Locate every uninfected red blood cell.
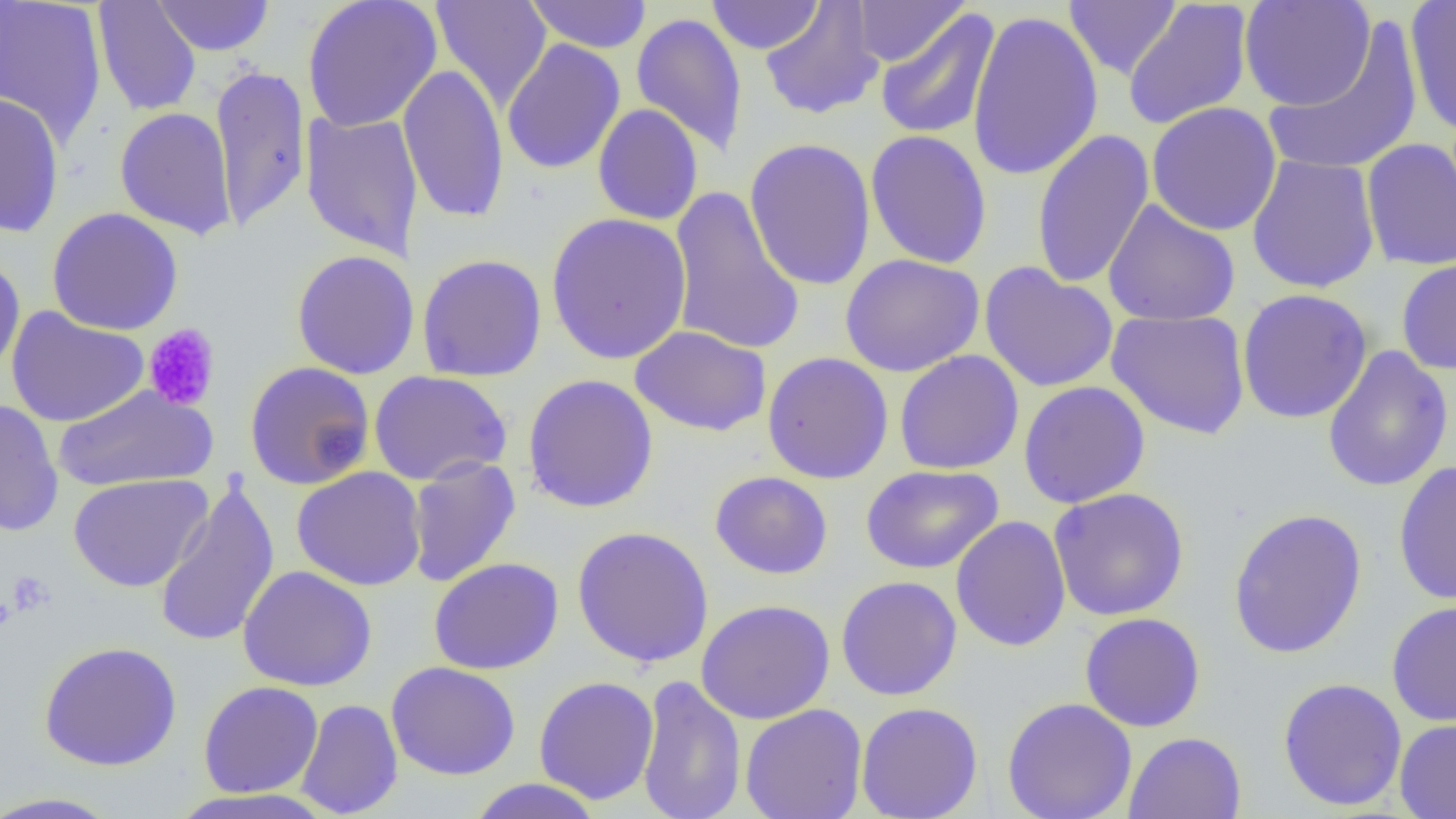
Approximate bounding boxes as [x1, y1, x2, y2] in pixels.
Uninfected red blood cells: [92, 0, 202, 117], [152, 0, 275, 56], [302, 0, 442, 132], [431, 0, 551, 111], [524, 0, 653, 53], [705, 0, 824, 54], [1064, 0, 1181, 80], [1239, 0, 1375, 111], [1404, 0, 1456, 138], [0, 1, 108, 146], [759, 1, 885, 120], [851, 1, 968, 67], [1122, 1, 1254, 131], [875, 8, 1001, 141], [966, 9, 1104, 182], [630, 13, 748, 158], [1263, 19, 1423, 179], [501, 39, 626, 175], [397, 63, 510, 224], [209, 64, 311, 231], [0, 91, 65, 238], [1146, 101, 1282, 236], [592, 104, 704, 226], [114, 107, 236, 239], [300, 112, 423, 260], [1031, 128, 1155, 290], [865, 129, 993, 270], [744, 137, 877, 292], [1361, 138, 1456, 271], [1246, 154, 1381, 294], [667, 185, 805, 356], [1103, 198, 1241, 327], [46, 207, 184, 336], [546, 212, 692, 365], [291, 250, 420, 379], [416, 253, 547, 382], [840, 253, 984, 377], [0, 255, 26, 381], [1396, 256, 1456, 376], [978, 262, 1119, 393], [1237, 288, 1373, 424], [6, 307, 150, 427], [1106, 309, 1250, 439], [630, 325, 772, 437], [1322, 346, 1453, 493], [893, 349, 1024, 474], [761, 351, 894, 484], [244, 361, 376, 490], [369, 370, 512, 485], [522, 373, 659, 513], [1018, 380, 1151, 508], [53, 384, 218, 491], [0, 399, 64, 537], [405, 456, 521, 588], [1393, 460, 1456, 606], [861, 464, 1003, 575], [291, 466, 427, 591], [710, 470, 833, 579], [69, 473, 212, 592], [154, 479, 281, 648], [1048, 486, 1190, 621], [1227, 507, 1367, 659], [950, 516, 1071, 652], [572, 525, 714, 668], [428, 557, 564, 674], [238, 565, 377, 691], [835, 575, 963, 701], [696, 599, 835, 724], [1386, 600, 1456, 727], [1079, 612, 1206, 732], [38, 641, 182, 771], [386, 661, 520, 780], [635, 674, 747, 819], [533, 676, 660, 805], [1277, 677, 1408, 811], [198, 681, 323, 798], [1002, 696, 1138, 819], [295, 698, 403, 818], [855, 702, 984, 819], [740, 703, 868, 819], [1394, 717, 1456, 818], [1124, 731, 1246, 819], [467, 778, 603, 819], [167, 789, 333, 819], [0, 791, 124, 818].

Summary:
  - Platelet locations: [143, 324, 220, 411], [5, 570, 56, 617]
  - Slide-level diagnosis: negative for blood parasites
  - Modality: optical microscopy
  - Image size: 1456×819 pixels
  - Field of view: single
  - Preparation: thin blood smear
  - Magnification: 1000x